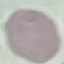

result: negative for malaria parasites
stain: Giemsa
preparation: thin blood smear
capture: smartphone camera at the microscope eyepiece
image_type: automatically extracted cell patch, resized to 64 × 64 pixels